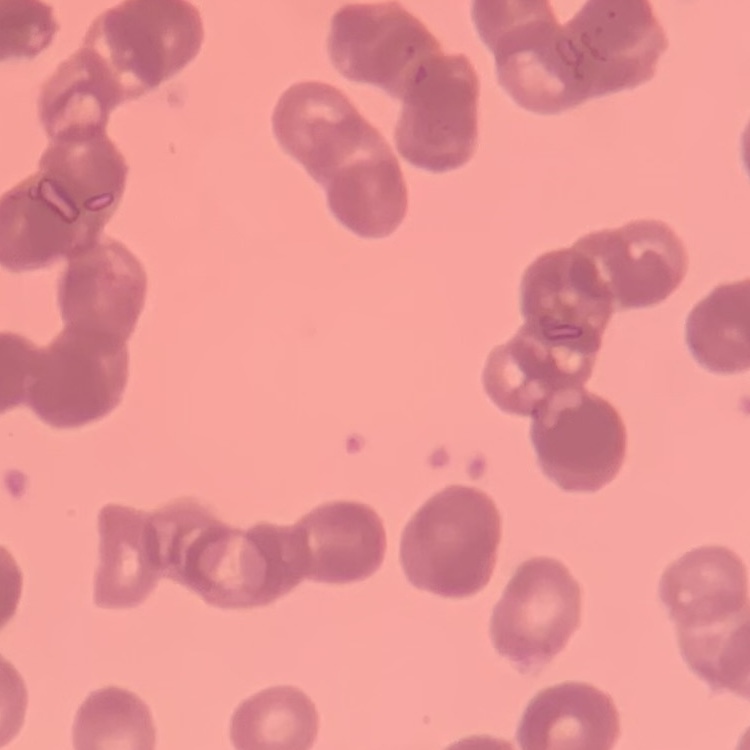

Summary:
  - Red blood cell morphology: rouleaux formation
  - Stain: Field's or Giemsa
  - Preparation: thin peripheral smear
  - Image type: square crop of a larger photomicrograph